State which cell type is depicted.
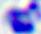

A leukocyte.

Micrograph. 400x magnification.